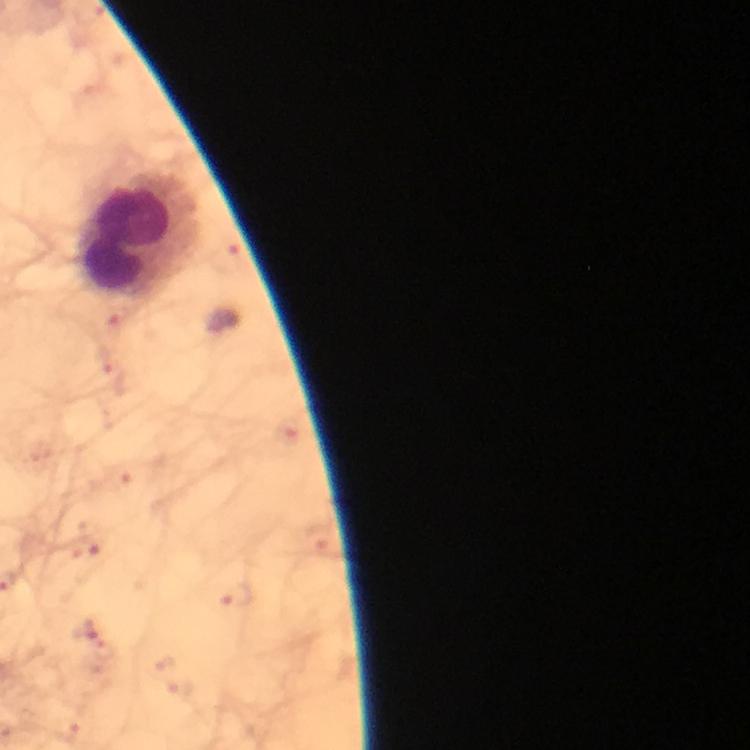

capture = smartphone camera through the microscope
magnification = 100x
stain = Giemsa
context = from a malaria diagnostic workup
cropped from = one field of view
malaria parasites = none seen
leukocyte locations = approximate centers as [x, y] in pixels: [142, 240]
image size = 750×750 pixels
preparation = thick blood film
immersion oil = applied